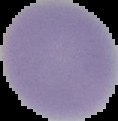

The area outside the segmented cell region is set to black. Malaria status: uninfected. Image is 118×121 pixels. From a thin blood film.